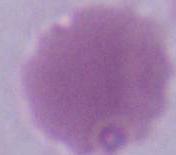

{
  "modality": "photomicrograph",
  "magnification": "1000x",
  "identification": "erythrocyte"
}